Mark where platelets are.
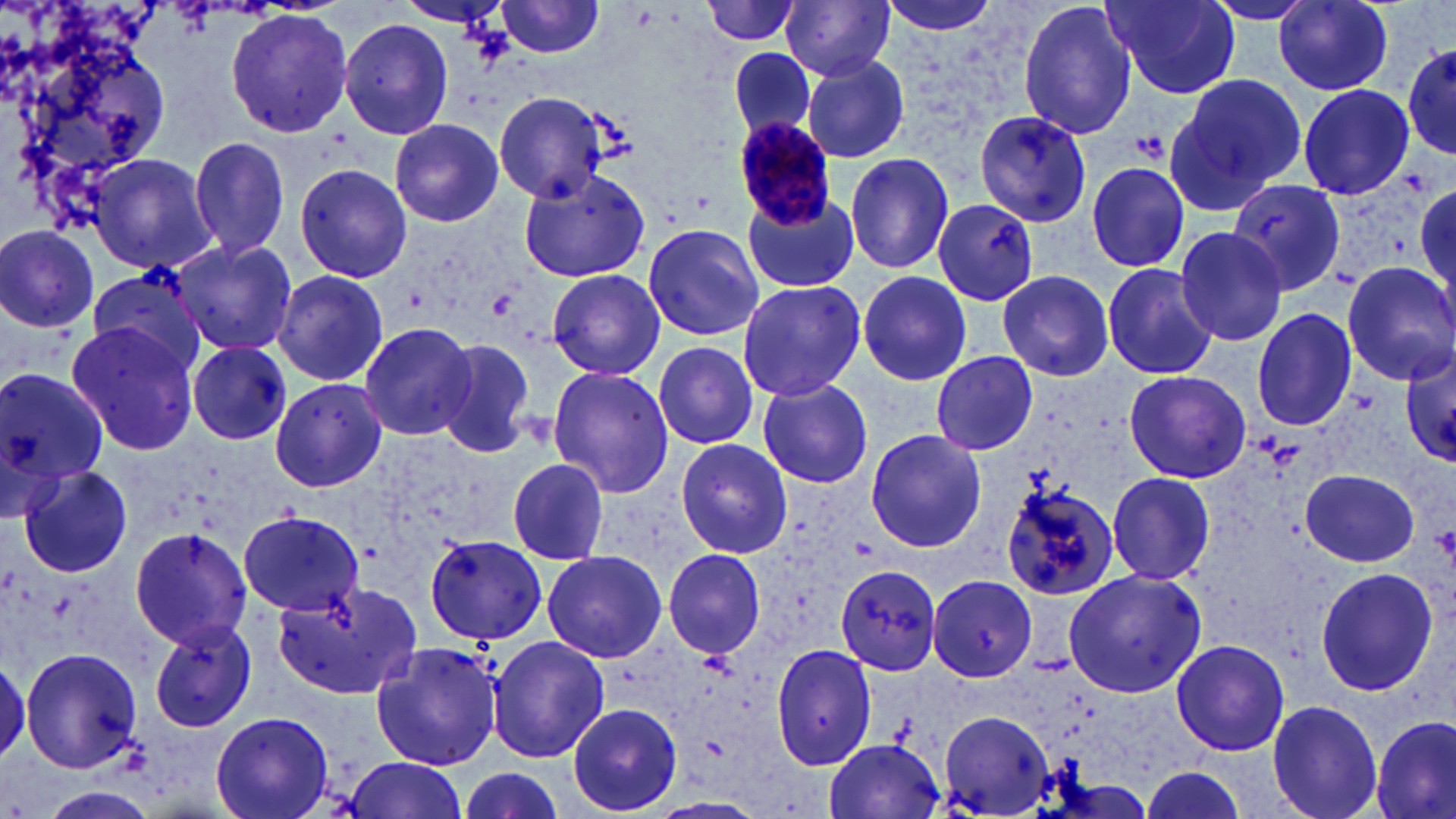

Approximate bounding boxes as [x1, y1, x2, y2] in pixels.
Platelets: [1130, 131, 1168, 161], [484, 289, 523, 322], [1432, 523, 1456, 567].

Plasmodium malariae-infected red blood cell locations: [732, 117, 840, 228]. Uninfected red blood cell locations: [389, 0, 527, 34], [783, 0, 896, 82], [872, 0, 1003, 36], [1017, 0, 1139, 141], [1104, 0, 1241, 99], [1205, 0, 1318, 24], [1276, 0, 1395, 95], [496, 1, 607, 58], [700, 1, 803, 47], [6, 6, 169, 204], [226, 9, 356, 137], [338, 17, 453, 139], [1399, 35, 1454, 166], [727, 46, 820, 143], [800, 58, 910, 163], [1167, 72, 1308, 207], [1297, 84, 1415, 201], [493, 92, 612, 205], [973, 110, 1092, 227], [388, 118, 504, 227], [188, 135, 291, 262], [843, 152, 955, 274], [88, 153, 217, 273], [1084, 160, 1192, 274], [294, 161, 412, 283], [513, 166, 655, 281], [1232, 178, 1345, 294], [1414, 182, 1456, 309], [742, 190, 860, 293], [916, 200, 1043, 343], [641, 223, 764, 342], [0, 224, 101, 332], [1172, 225, 1287, 347], [170, 240, 298, 354], [1342, 261, 1456, 384], [1101, 263, 1217, 381], [83, 265, 210, 378], [273, 268, 390, 387], [546, 268, 664, 381], [997, 268, 1116, 383], [857, 270, 973, 387], [736, 279, 865, 401], [1251, 307, 1356, 431], [66, 320, 201, 455], [358, 321, 480, 442], [431, 338, 540, 459], [189, 342, 290, 445], [650, 343, 762, 452], [1400, 344, 1456, 467], [931, 350, 1039, 456], [0, 363, 108, 504], [546, 366, 674, 499], [1123, 370, 1250, 484], [756, 376, 874, 489], [270, 377, 387, 493], [864, 428, 987, 554], [674, 438, 793, 558], [505, 457, 612, 565], [18, 466, 134, 578], [1300, 468, 1421, 568], [1107, 471, 1216, 586], [1000, 481, 1122, 600], [239, 512, 365, 616], [125, 526, 253, 650], [424, 535, 548, 644], [664, 548, 766, 659], [541, 550, 666, 663], [835, 564, 942, 675], [1064, 568, 1208, 699], [1315, 568, 1439, 695], [925, 573, 1039, 681], [274, 580, 419, 702], [150, 619, 257, 734], [485, 637, 610, 764], [1169, 638, 1290, 756], [370, 641, 505, 772], [771, 642, 877, 772], [20, 647, 143, 773], [0, 658, 28, 763], [1267, 699, 1383, 819], [568, 703, 682, 815], [937, 709, 1055, 816], [210, 712, 334, 819], [1371, 716, 1455, 819], [825, 737, 944, 818], [343, 757, 468, 819], [1135, 762, 1252, 819], [456, 766, 570, 819]. Slide-level diagnosis: Plasmodium malariae. Captured at 1000x magnification. Optical microscopy. Image is 1456×819 pixels. Thin blood film. May-Grünwald-Giemsa-stained preparation. One field of a larger specimen.